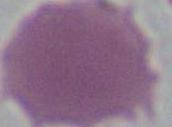 A red blood cell is seen. Photomicrograph. 1000x magnification.